Classify this cell by malaria status.
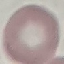
Uninfected.

image type = automatically extracted cell patch, resized to 64 × 64 pixels
stain = Giemsa
capture = smartphone camera at the microscope eyepiece
preparation = thin smear